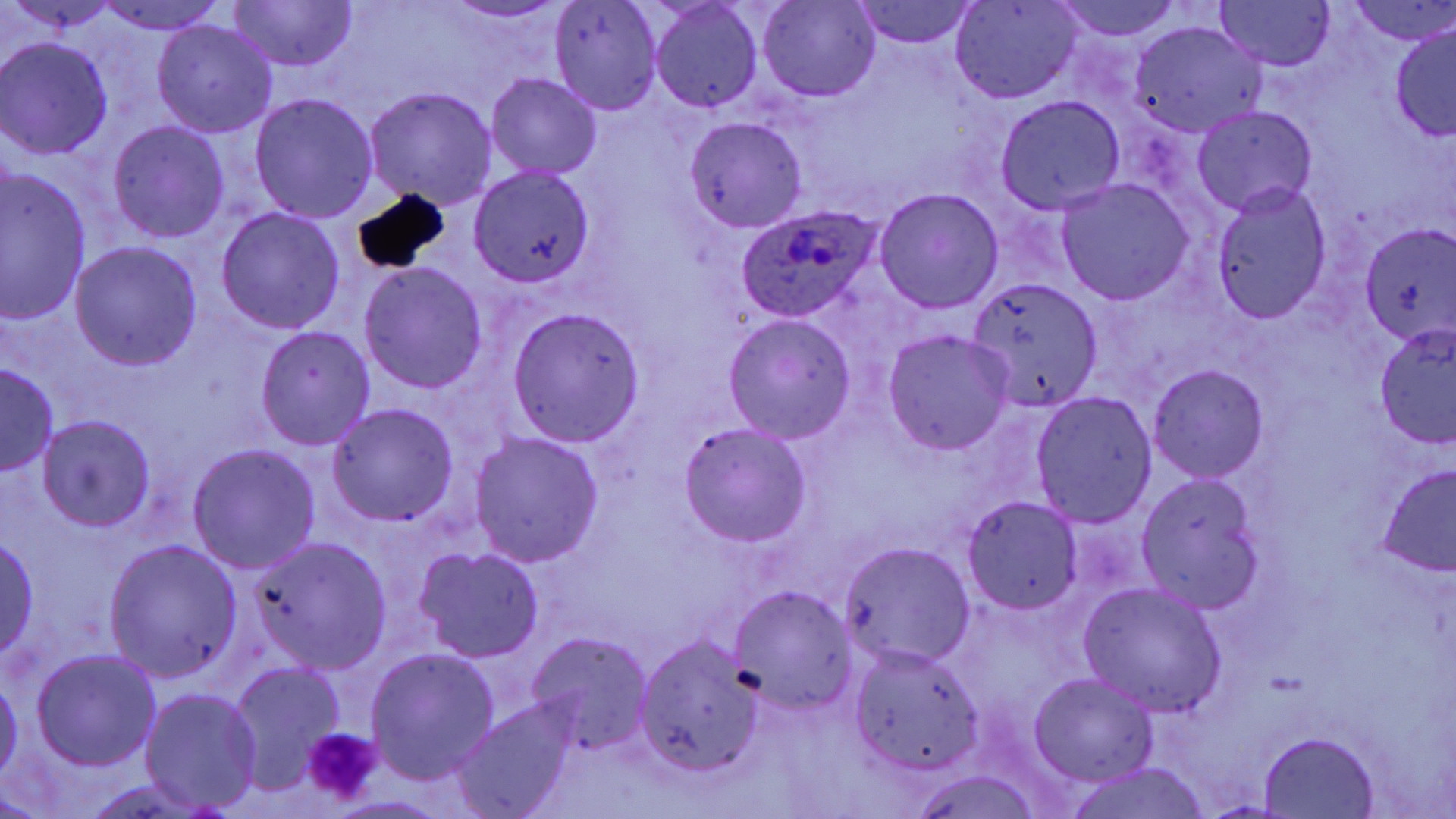

{
  "slide_level_diagnosis": "Plasmodium ovale",
  "field_of_view": "one of a larger specimen",
  "preparation": "thin blood smear",
  "uninfected_red_blood_cell_locations": "approximate bounding boxes as [x1, y1, x2, y2] in pixels: [11, 0, 119, 35], [439, 0, 574, 24], [757, 0, 879, 101], [1048, 0, 1189, 42], [1216, 0, 1335, 71], [1350, 0, 1456, 47], [97, 1, 226, 36], [226, 1, 357, 72], [951, 1, 1081, 102], [551, 2, 663, 116], [851, 2, 978, 49], [650, 3, 763, 113], [152, 19, 278, 139], [1128, 20, 1268, 140], [1390, 23, 1456, 142], [0, 36, 116, 159], [486, 72, 601, 179], [363, 86, 497, 208], [249, 92, 379, 222], [995, 95, 1126, 214], [1194, 105, 1317, 216], [684, 116, 808, 233], [108, 120, 230, 244], [470, 167, 595, 286], [1, 169, 93, 324], [1056, 179, 1194, 304], [1211, 184, 1331, 322], [874, 188, 1004, 314], [216, 205, 346, 334], [70, 241, 202, 370], [359, 261, 489, 395], [966, 277, 1103, 411], [507, 307, 644, 445], [723, 315, 858, 443], [1374, 324, 1455, 448], [256, 326, 376, 449], [883, 330, 1014, 455], [0, 362, 58, 476], [1147, 363, 1269, 482], [1031, 392, 1157, 527], [326, 403, 459, 526], [38, 415, 156, 532], [679, 423, 813, 546], [469, 431, 603, 567], [189, 444, 320, 575], [1375, 462, 1456, 581], [1137, 475, 1266, 611], [962, 498, 1084, 615], [0, 535, 40, 660], [251, 537, 391, 673], [104, 539, 241, 682], [838, 542, 975, 670], [414, 547, 544, 662], [1078, 581, 1228, 717], [729, 586, 856, 713], [527, 632, 653, 757], [635, 636, 762, 776], [850, 647, 983, 777], [365, 648, 500, 782], [33, 650, 163, 770], [226, 662, 344, 791], [1029, 671, 1158, 787], [0, 677, 22, 786], [142, 688, 264, 813], [454, 700, 574, 818], [1259, 731, 1378, 817], [1064, 763, 1213, 819], [903, 769, 1048, 819]",
  "modality": "optical microscopy",
  "plasmodium_ovale_infected_red_blood_cell_locations": "approximate bounding boxes as [x1, y1, x2, y2] in pixels: [736, 203, 885, 322], [1361, 227, 1456, 341]",
  "platelet_locations": "approximate bounding boxes as [x1, y1, x2, y2] in pixels: [301, 727, 380, 805]",
  "magnification": "1000x",
  "image_size": "1456×819 pixels",
  "stain": "May-Grünwald-Giemsa"
}